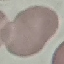

Result: negative for malaria parasites. Acquired by smartphone through the microscope eyepiece. Thin smear of blood. Giemsa-stained preparation. Automatically extracted cell patch, resized to 64 × 64 pixels.